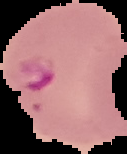
Summary:
  - Image type: segmented cell region on a black background
  - Image size: 127×154 pixels
  - Result: malaria parasites detected
  - Preparation: thin blood film